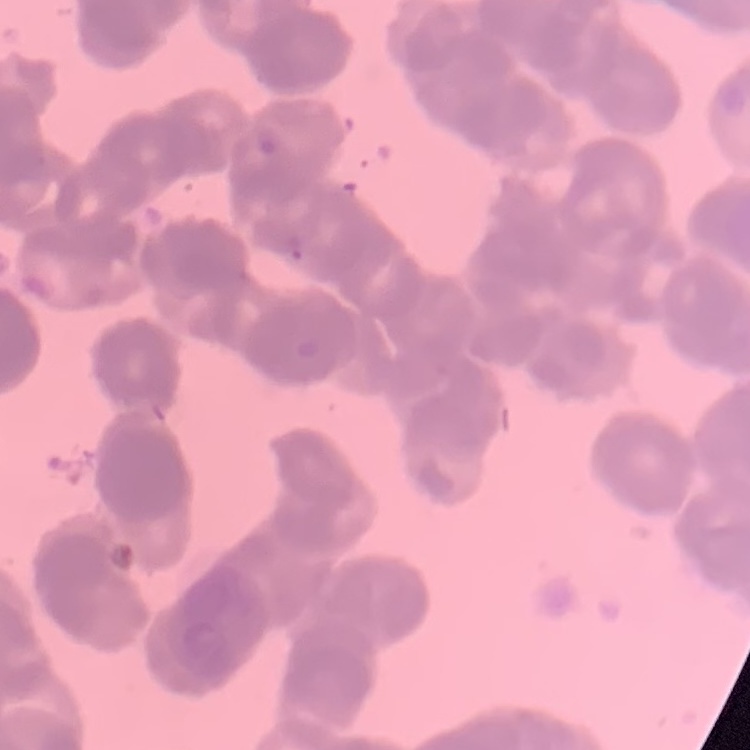
{
  "red_blood_cell_morphology": "rouleaux formation",
  "preparation": "thin peripheral smear",
  "stain": "Field's or Giemsa",
  "image_type": "square crop of a larger photomicrograph"
}